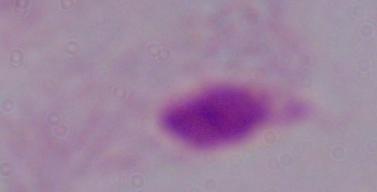

1000x magnification. Photomicrograph. A trichomonad is shown.